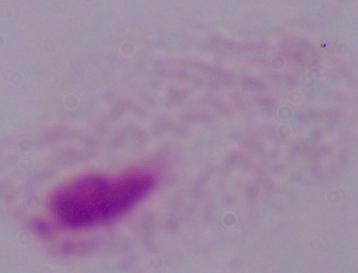

magnification = 1000x
modality = micrograph
identification = trichomonad